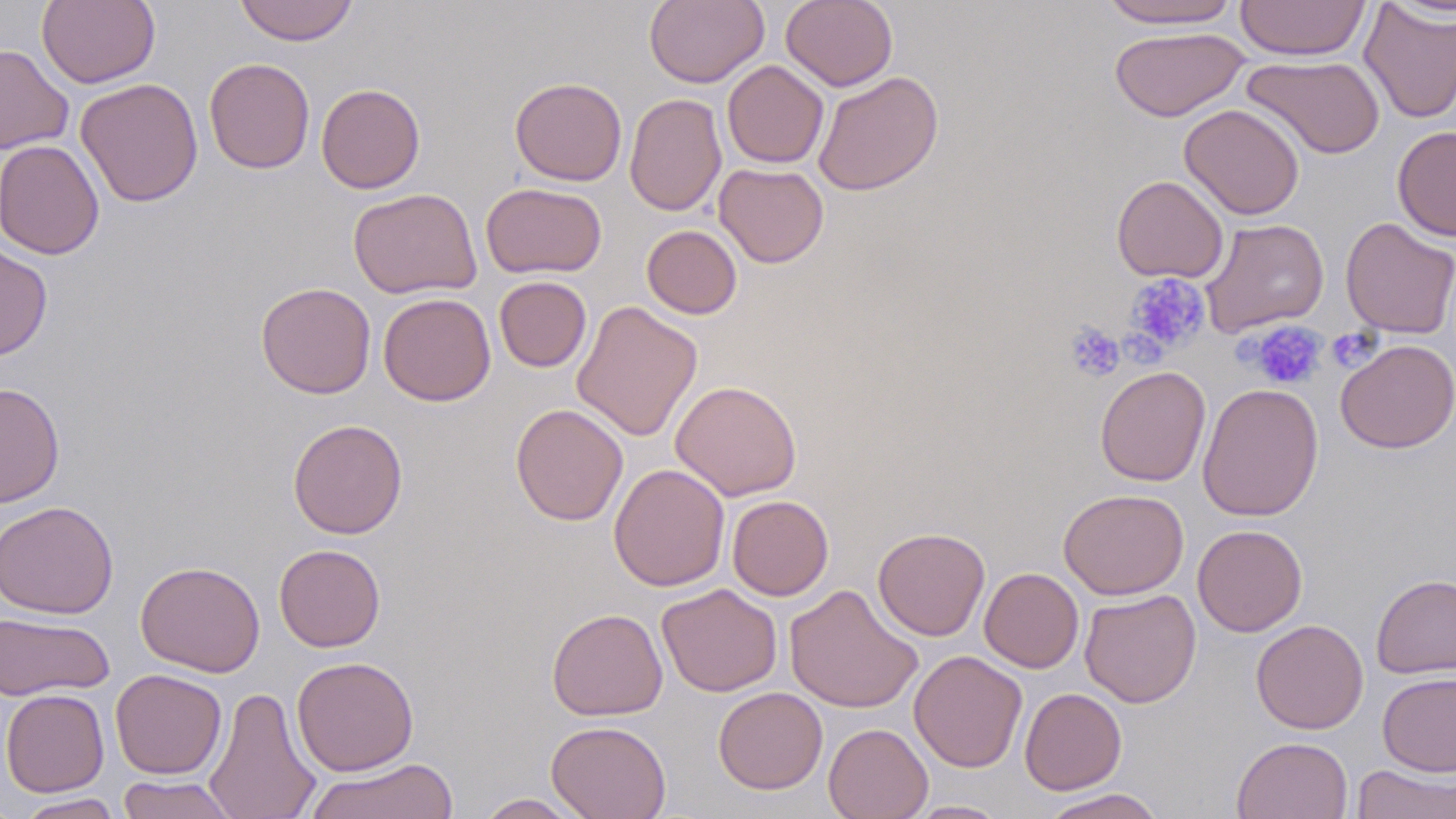

Approximate bounding boxes as (x1, y1, x2, y2) in pixels. Uninfected red blood cell locations: (37, 0, 160, 89), (234, 0, 359, 46), (644, 0, 769, 88), (781, 0, 898, 91), (1096, 0, 1243, 29), (1235, 0, 1371, 61), (1359, 3, 1456, 123), (1109, 27, 1249, 122), (0, 43, 74, 154), (1242, 54, 1385, 159), (204, 57, 314, 174), (722, 60, 829, 168), (813, 70, 944, 196), (76, 77, 203, 207), (510, 77, 628, 186), (316, 83, 425, 194), (624, 93, 727, 216), (1179, 103, 1305, 220), (1392, 125, 1456, 241), (1, 138, 104, 260), (714, 163, 828, 268), (1111, 175, 1229, 283), (481, 182, 607, 279), (348, 187, 482, 299), (1340, 216, 1456, 339), (1199, 218, 1329, 337), (642, 224, 742, 319), (0, 242, 53, 361), (494, 276, 592, 372), (256, 281, 376, 398), (378, 292, 496, 406), (572, 300, 703, 442), (1335, 339, 1456, 453), (1095, 365, 1211, 486), (671, 380, 802, 501), (1, 382, 65, 508), (1197, 382, 1324, 522), (510, 403, 629, 526), (287, 419, 408, 540), (609, 463, 730, 591), (1058, 488, 1189, 600), (727, 495, 834, 601), (0, 500, 118, 619), (1192, 524, 1308, 637), (873, 527, 990, 640), (273, 544, 386, 652), (134, 560, 265, 678), (979, 567, 1084, 673), (1371, 573, 1456, 679), (656, 583, 783, 698), (784, 583, 923, 713), (1079, 589, 1202, 708), (546, 607, 668, 721), (0, 611, 114, 701), (1251, 618, 1369, 734), (909, 650, 1027, 772), (292, 656, 419, 776), (110, 669, 227, 779), (1377, 672, 1456, 776), (203, 685, 322, 819), (713, 686, 827, 794), (1019, 688, 1127, 795), (1, 689, 109, 797), (546, 720, 671, 819), (823, 723, 933, 819), (1232, 736, 1353, 818), (302, 757, 459, 819), (1351, 763, 1455, 818), (116, 775, 240, 818), (1039, 788, 1169, 818), (474, 793, 589, 818), (15, 794, 124, 819), (905, 800, 1010, 818). Platelet locations: (1125, 274, 1211, 356), (1245, 320, 1328, 390), (1064, 322, 1125, 382), (1325, 327, 1381, 370), (1125, 334, 1166, 368). Slide-level diagnosis: no evidence of blood parasites. Thin blood film. Single field of view. Captured at 1000x magnification. Image is 1456×819 pixels. May-Grünwald-Giemsa-stained preparation. Optical microscopy.